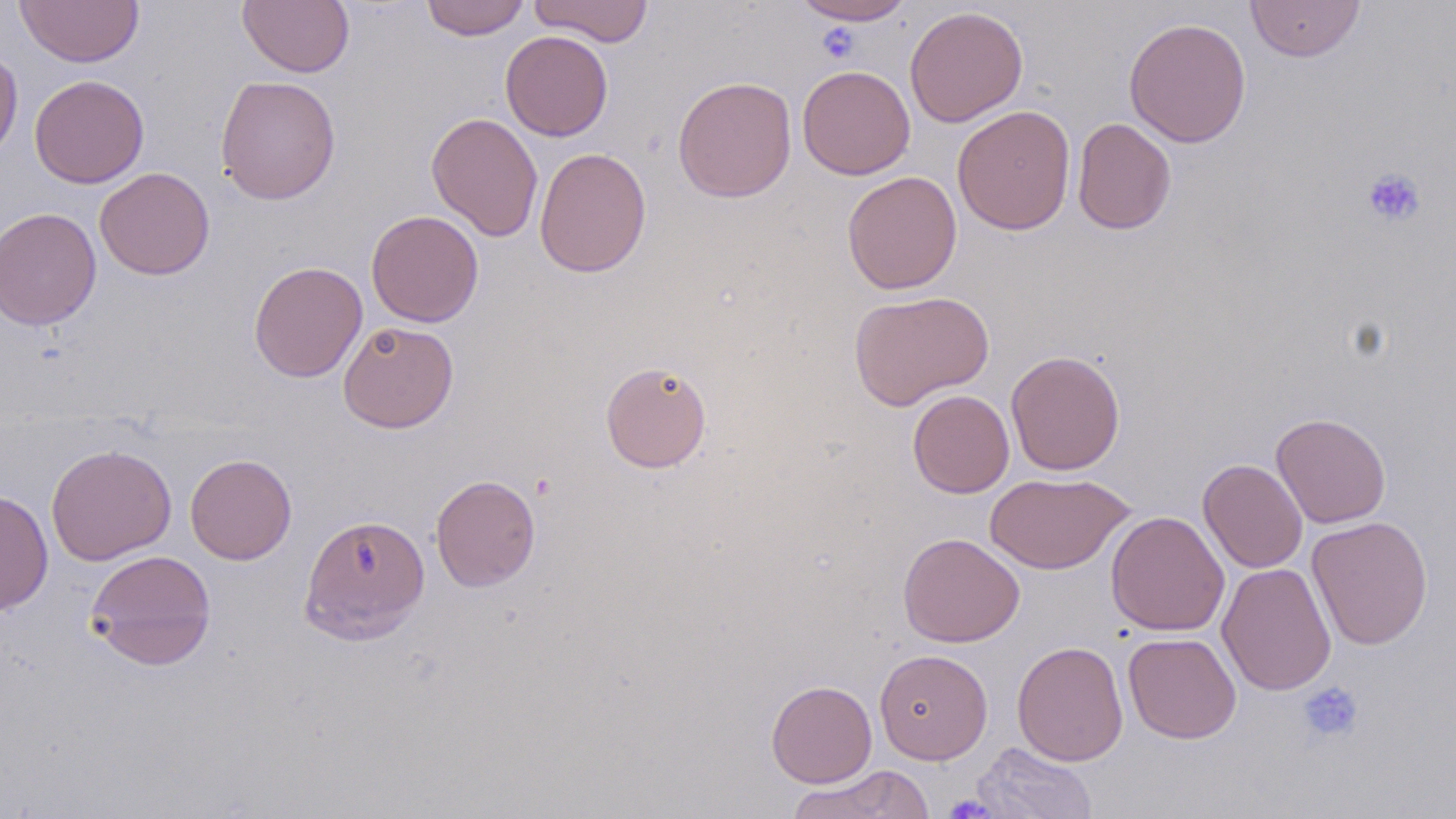

slide-level diagnosis = no evidence of blood parasites
magnification = 1000x
platelet locations = approximate bounding boxes as named x1/y1/x2/y2 corners in pixels: (x1=818, y1=25, x2=861, y2=63), (x1=1362, y1=167, x2=1425, y2=227), (x1=1297, y1=681, x2=1365, y2=743), (x1=943, y1=795, x2=999, y2=819)
preparation = thin blood film
uninfected red blood cell locations = approximate bounding boxes as named x1/y1/x2/y2 corners in pixels: (x1=14, y1=0, x2=144, y2=67), (x1=238, y1=0, x2=354, y2=78), (x1=419, y1=0, x2=530, y2=40), (x1=529, y1=0, x2=655, y2=46), (x1=790, y1=0, x2=916, y2=25), (x1=1245, y1=0, x2=1366, y2=62), (x1=904, y1=6, x2=1028, y2=127), (x1=1124, y1=17, x2=1252, y2=148), (x1=500, y1=30, x2=613, y2=141), (x1=0, y1=47, x2=23, y2=163), (x1=796, y1=65, x2=915, y2=180), (x1=29, y1=74, x2=149, y2=189), (x1=215, y1=75, x2=341, y2=204), (x1=672, y1=75, x2=797, y2=203), (x1=953, y1=105, x2=1076, y2=235), (x1=426, y1=112, x2=543, y2=242), (x1=1072, y1=118, x2=1176, y2=235), (x1=534, y1=147, x2=651, y2=277), (x1=95, y1=167, x2=215, y2=280), (x1=842, y1=170, x2=962, y2=295), (x1=0, y1=207, x2=101, y2=331), (x1=366, y1=210, x2=484, y2=327), (x1=248, y1=260, x2=367, y2=382), (x1=848, y1=289, x2=994, y2=411), (x1=338, y1=320, x2=458, y2=433), (x1=1005, y1=349, x2=1125, y2=475), (x1=600, y1=360, x2=712, y2=473), (x1=907, y1=389, x2=1014, y2=498), (x1=1271, y1=412, x2=1391, y2=528), (x1=46, y1=443, x2=177, y2=565), (x1=184, y1=453, x2=297, y2=565), (x1=1198, y1=458, x2=1307, y2=573), (x1=984, y1=471, x2=1135, y2=575), (x1=430, y1=474, x2=541, y2=592), (x1=0, y1=489, x2=53, y2=615), (x1=1105, y1=510, x2=1229, y2=636), (x1=299, y1=514, x2=430, y2=643), (x1=1307, y1=515, x2=1433, y2=650), (x1=898, y1=532, x2=1025, y2=647), (x1=86, y1=549, x2=217, y2=670), (x1=1217, y1=562, x2=1337, y2=696), (x1=1123, y1=632, x2=1241, y2=744), (x1=1011, y1=640, x2=1128, y2=766), (x1=874, y1=649, x2=993, y2=764), (x1=766, y1=680, x2=877, y2=787), (x1=972, y1=742, x2=1098, y2=819), (x1=785, y1=764, x2=935, y2=819)
field of view = single
image size = 1456×819 pixels
modality = light microscopy
stain = May-Grünwald-Giemsa